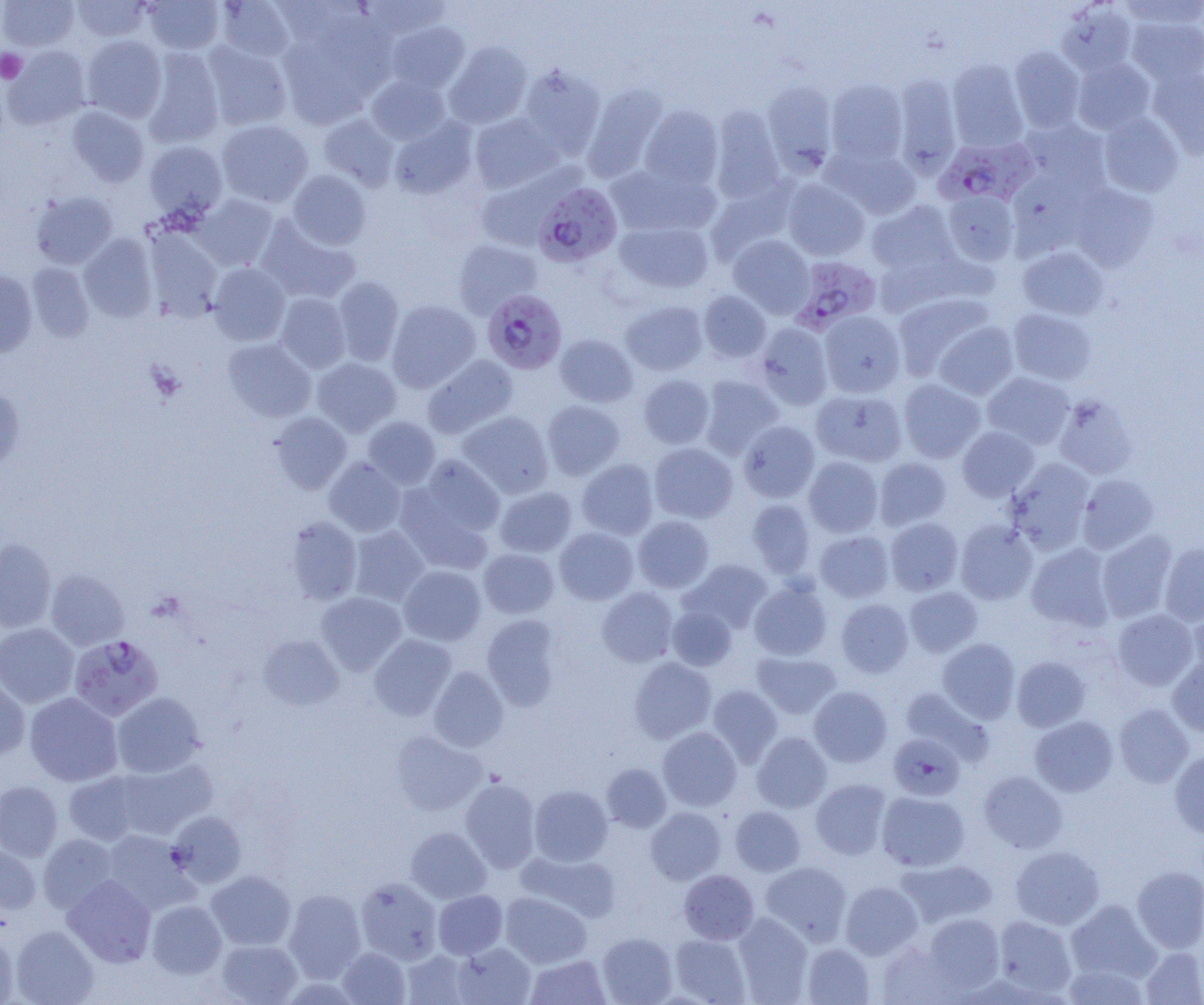

slide-level diagnosis = Plasmodium falciparum
field of view = one of a larger specimen
modality = optical microscopy
preparation = thin blood film
Plasmodium falciparum-infected red blood cell locations = approximate bounding boxes as (x1, y1, x2, y2) in pixels: (935, 137, 1037, 207), (533, 182, 622, 266), (791, 256, 882, 332), (482, 289, 567, 374), (69, 634, 163, 721), (888, 733, 965, 801)
platelet locations = approximate bounding boxes as (x1, y1, x2, y2) in pixels: (0, 48, 27, 83), (146, 361, 185, 403)
magnification = 1000x
uninfected red blood cell locations = approximate bounding boxes as (x1, y1, x2, y2) in pixels: (0, 0, 78, 51), (72, 0, 152, 42), (142, 0, 225, 54), (356, 0, 453, 39), (1119, 0, 1204, 30), (215, 1, 296, 61), (1056, 2, 1137, 77), (1127, 14, 1204, 86), (385, 21, 470, 93), (276, 26, 386, 129), (81, 35, 166, 122), (202, 41, 292, 131), (444, 41, 532, 129), (3, 46, 92, 130), (1009, 46, 1085, 132), (143, 48, 225, 148), (1072, 57, 1156, 134), (947, 59, 1028, 151), (518, 64, 605, 156), (1149, 68, 1204, 158), (892, 74, 962, 177), (366, 75, 450, 145), (826, 78, 908, 165), (761, 79, 839, 173), (581, 83, 669, 182), (67, 105, 149, 187), (639, 105, 723, 189), (709, 105, 785, 202), (1098, 112, 1184, 197), (469, 113, 563, 193), (318, 114, 400, 190), (389, 117, 478, 199), (1019, 118, 1110, 192), (216, 120, 313, 207), (143, 141, 227, 220), (825, 145, 921, 220), (607, 163, 720, 238), (479, 167, 593, 239), (287, 170, 371, 250), (782, 179, 869, 260), (706, 180, 795, 263), (1069, 182, 1160, 270), (30, 191, 117, 269), (942, 191, 1018, 265), (193, 194, 279, 270), (866, 200, 958, 278), (256, 216, 360, 305), (615, 220, 714, 293), (145, 229, 222, 321), (79, 234, 158, 322), (728, 235, 814, 317), (453, 239, 543, 318), (1017, 247, 1109, 321), (27, 262, 94, 342), (208, 262, 290, 346), (0, 270, 37, 357), (333, 276, 404, 366), (698, 290, 772, 362), (893, 292, 996, 380), (275, 293, 351, 373), (386, 299, 480, 392), (621, 300, 708, 376), (1008, 307, 1096, 385), (819, 310, 906, 397), (932, 321, 1018, 400), (754, 323, 833, 409), (555, 334, 638, 407), (222, 338, 316, 422), (423, 355, 518, 439), (312, 358, 401, 436), (982, 372, 1075, 449), (638, 375, 714, 448), (698, 375, 782, 459), (898, 378, 985, 463), (0, 386, 24, 470), (811, 388, 908, 467), (1053, 395, 1137, 479), (542, 400, 625, 480), (270, 411, 351, 493), (458, 411, 553, 498), (362, 416, 440, 488), (738, 420, 819, 502), (957, 426, 1039, 501), (649, 443, 738, 523), (412, 455, 505, 540), (804, 457, 883, 537), (874, 457, 951, 530), (324, 458, 406, 537), (1006, 458, 1095, 553), (577, 459, 659, 539), (1077, 474, 1158, 554), (494, 486, 577, 557), (747, 499, 815, 577), (633, 515, 714, 593), (285, 516, 362, 604), (885, 518, 963, 595), (955, 521, 1038, 604), (348, 526, 429, 606), (554, 527, 638, 605), (1097, 529, 1178, 622), (815, 531, 894, 602), (0, 539, 56, 632), (1160, 542, 1204, 625), (1026, 543, 1115, 631), (478, 548, 559, 619), (682, 559, 773, 634), (399, 565, 486, 646), (45, 569, 129, 650), (749, 582, 832, 660), (905, 586, 983, 657), (596, 587, 678, 667), (317, 592, 407, 674), (836, 599, 914, 677), (1189, 604, 1204, 685), (667, 605, 737, 671), (1112, 608, 1199, 690), (481, 615, 563, 711), (0, 623, 79, 708), (257, 634, 344, 710), (369, 634, 456, 720), (937, 638, 1021, 723), (753, 651, 841, 718), (1012, 656, 1090, 731), (629, 657, 716, 743), (1167, 657, 1204, 737), (428, 666, 508, 752), (0, 675, 30, 761), (707, 685, 783, 766), (809, 686, 892, 767), (900, 687, 991, 763), (25, 692, 122, 786), (112, 692, 205, 778), (1114, 704, 1194, 788), (1030, 716, 1118, 796), (658, 727, 742, 810), (390, 731, 486, 815), (752, 732, 832, 812), (1169, 749, 1204, 838), (115, 758, 218, 839), (601, 763, 671, 832), (63, 770, 147, 846), (979, 771, 1068, 853), (810, 778, 891, 860), (460, 779, 540, 872), (0, 781, 63, 861), (529, 785, 612, 866), (876, 791, 970, 871), (646, 806, 726, 884), (730, 806, 805, 876), (168, 810, 247, 887), (406, 827, 491, 903), (101, 829, 196, 914), (38, 834, 118, 913), (0, 844, 41, 914), (1010, 845, 1105, 930), (518, 850, 621, 922), (895, 859, 998, 928), (760, 861, 852, 945), (1132, 866, 1204, 952), (206, 870, 296, 950), (680, 870, 758, 944), (63, 876, 156, 966), (356, 878, 442, 964), (840, 881, 923, 959), (284, 888, 366, 982), (433, 890, 507, 959), (500, 892, 591, 968), (147, 900, 226, 978), (1066, 900, 1160, 982), (732, 912, 813, 1003), (923, 913, 1005, 994), (993, 915, 1076, 997), (11, 925, 99, 1005), (0, 931, 19, 1004), (597, 933, 677, 1004), (670, 934, 751, 1004), (216, 939, 302, 1004), (877, 940, 960, 1005), (451, 942, 536, 1005), (802, 943, 875, 1004), (338, 947, 411, 1004), (1141, 947, 1204, 1005), (401, 949, 473, 1005), (526, 954, 610, 1004), (1063, 964, 1149, 1005)
image size = 1204×1005 pixels